Classify this cell by malaria status.
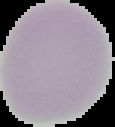

Uninfected.

Segmented cell region on a black background. Image is 115×127 pixels. From a thin blood smear.